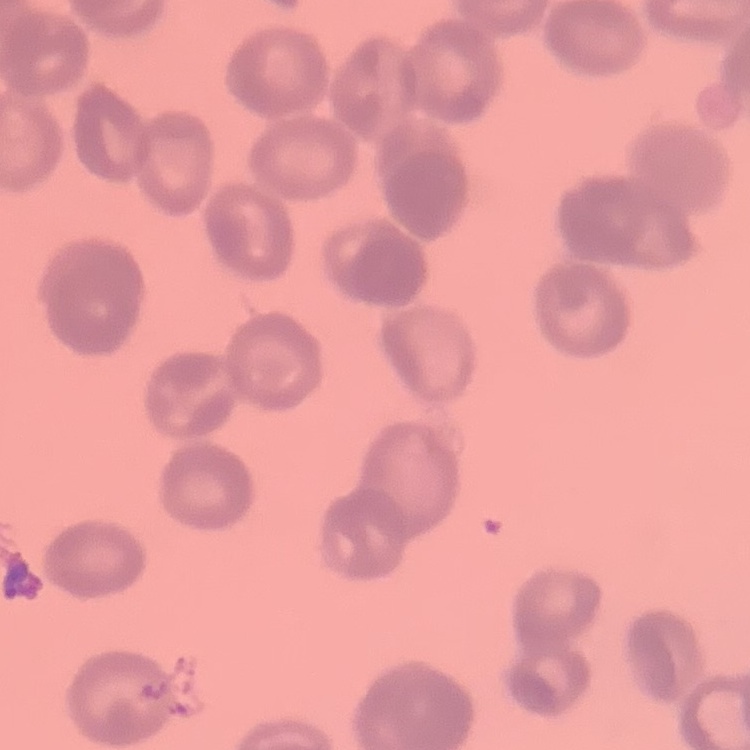
The erythrocytes show rouleaux formation. Stained with either Field's or Giemsa. One tile cut from a larger photomicrograph. Thin peripheral smear.